Classify this cell by malaria status.
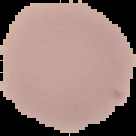
Uninfected.

From a thin blood film. Image is 136×136 pixels. Segmented cell region on a black background.